Name the parasite shown.
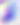
This is Toxoplasma gondii.

Captured at 400x magnification. Photomicrograph.